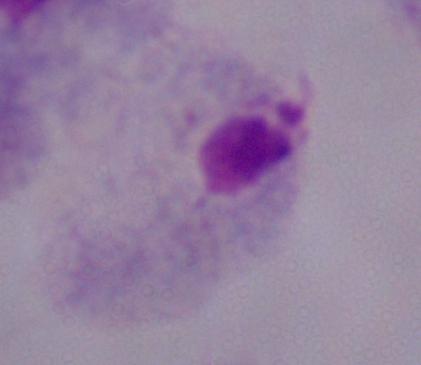
magnification = 1000x
modality = photomicrograph
identification = trichomonad